Name the parasite shown.
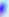

Toxoplasma gondii.

Summary:
  - Modality: photomicrograph
  - Magnification: 400x